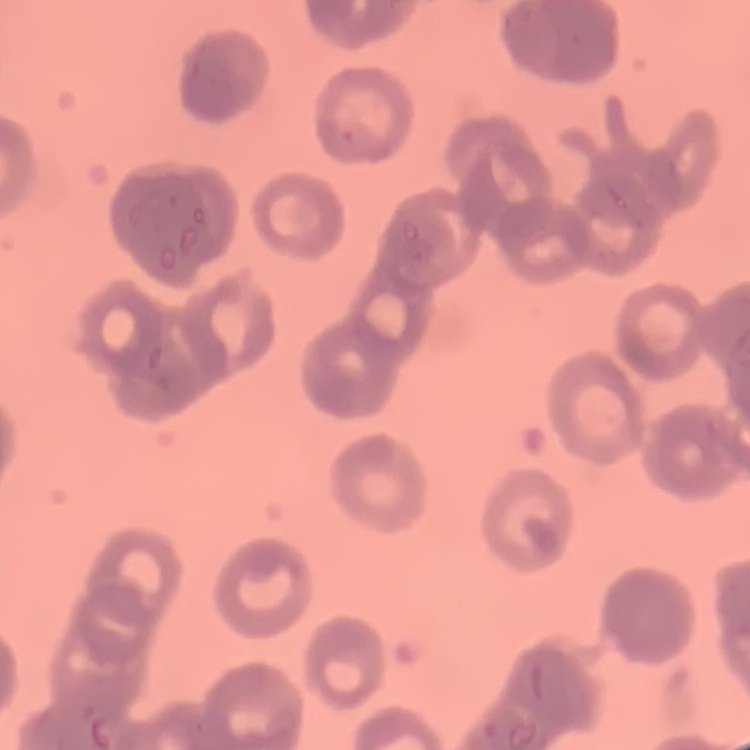
{
  "erythrocyte_morphology": "rouleaux formation",
  "stain": "Field's or Giemsa",
  "preparation": "thin blood film",
  "image_type": "one tile cut from a larger photomicrograph"
}